Name the parasite shown.
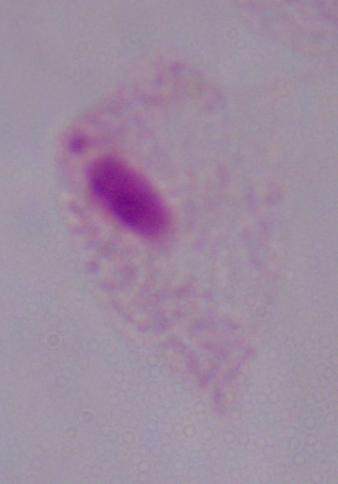
This is a trichomonad.

Photomicrograph. 1000x magnification.